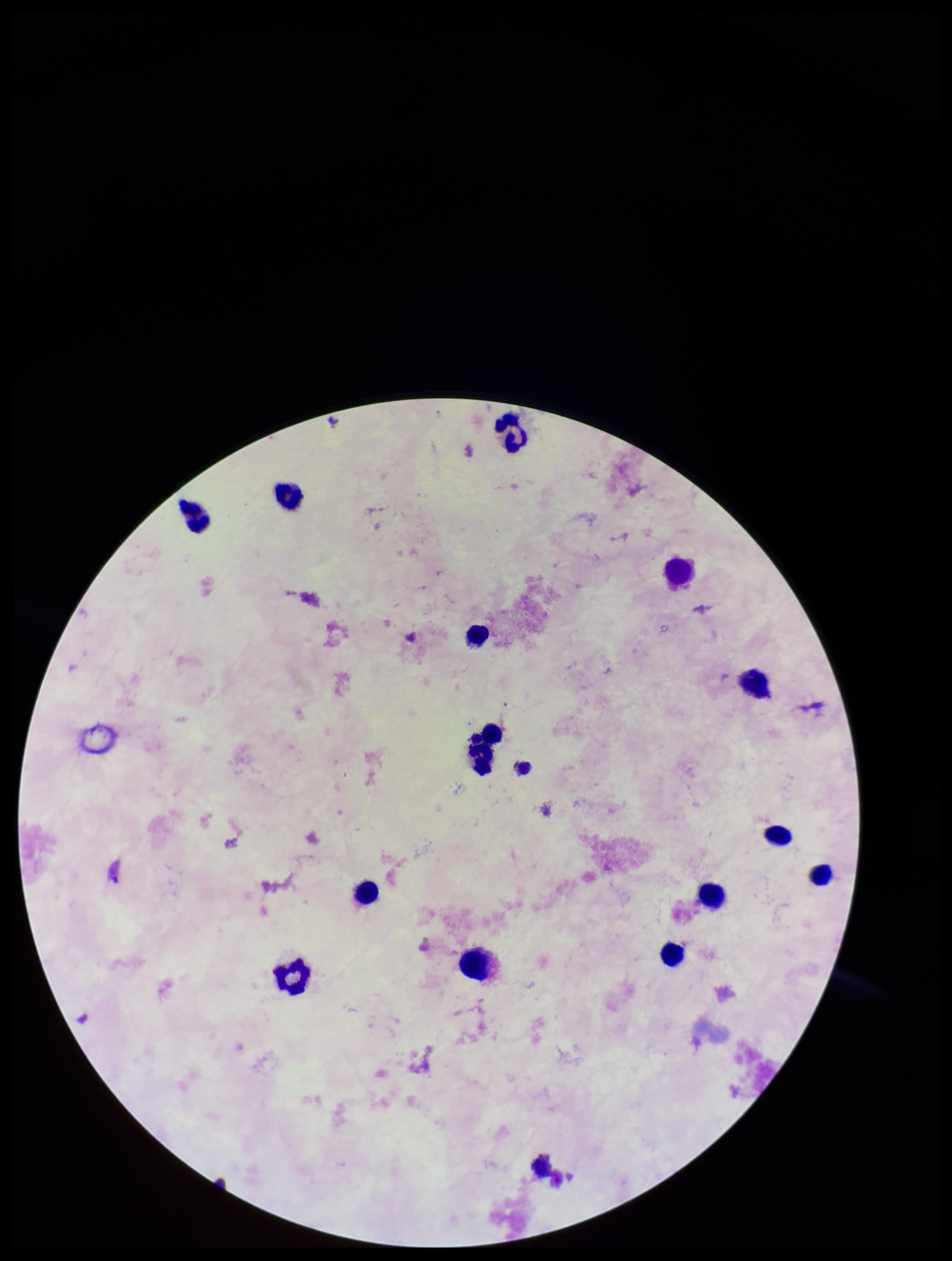

Single field of view. Image is 952×1261 pixels. Leukocyte count: 14. Plasmodium parasites: none identified. Parasite count: 0. Patient malaria status: negative. Preparation: thick blood smear. Photographed through the microscope eyepiece with a smartphone camera. Giemsa stain.